Name the parasite shown.
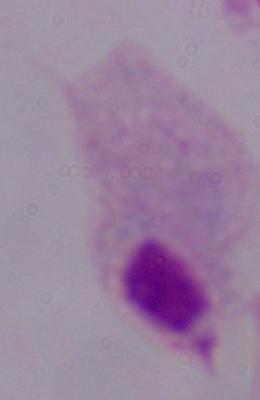

A trichomonad.

Summary:
  - Modality: micrograph
  - Magnification: 1000x